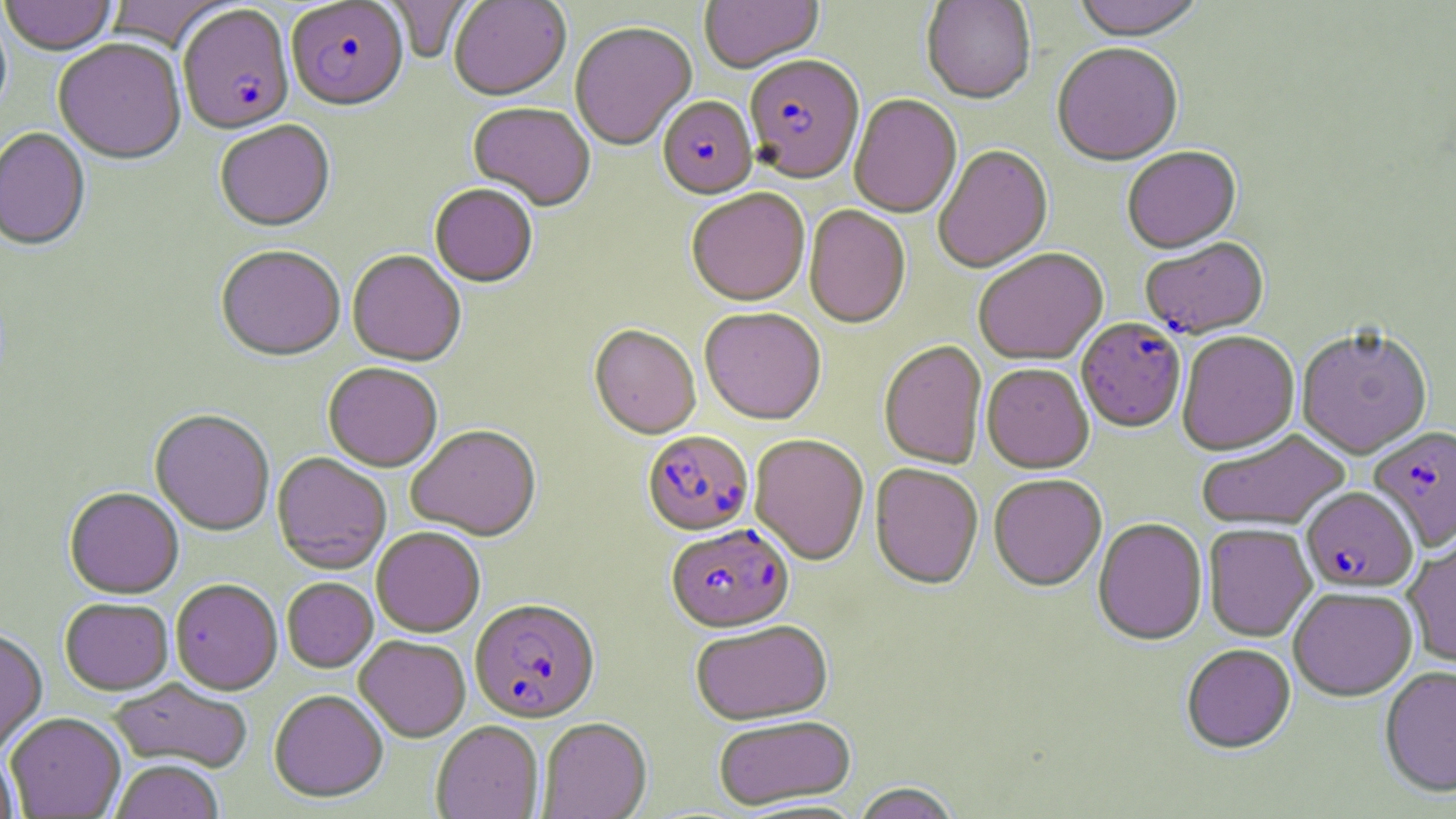
Approximate bounding boxes as named x1/y1/x2/y2 corners in pixels. Plasmodium falciparum-infected red blood cell locations: (x1=287, y1=2, x2=409, y2=114), (x1=178, y1=6, x2=295, y2=137), (x1=744, y1=57, x2=865, y2=186), (x1=657, y1=98, x2=757, y2=201), (x1=1141, y1=239, x2=1269, y2=341), (x1=1077, y1=319, x2=1186, y2=434), (x1=1368, y1=426, x2=1455, y2=553), (x1=642, y1=431, x2=754, y2=536), (x1=1301, y1=487, x2=1418, y2=594), (x1=667, y1=524, x2=794, y2=634), (x1=470, y1=600, x2=600, y2=724). Uninfected red blood cell locations: (x1=0, y1=0, x2=118, y2=57), (x1=107, y1=0, x2=236, y2=53), (x1=384, y1=0, x2=473, y2=62), (x1=449, y1=0, x2=571, y2=102), (x1=700, y1=0, x2=823, y2=75), (x1=921, y1=0, x2=1036, y2=106), (x1=1073, y1=0, x2=1205, y2=44), (x1=570, y1=23, x2=696, y2=152), (x1=53, y1=40, x2=187, y2=167), (x1=1052, y1=44, x2=1184, y2=169), (x1=849, y1=95, x2=962, y2=220), (x1=468, y1=104, x2=595, y2=213), (x1=215, y1=121, x2=335, y2=234), (x1=0, y1=129, x2=91, y2=253), (x1=934, y1=147, x2=1053, y2=274), (x1=1122, y1=148, x2=1242, y2=256), (x1=430, y1=186, x2=538, y2=289), (x1=686, y1=190, x2=810, y2=308), (x1=804, y1=206, x2=911, y2=330), (x1=215, y1=247, x2=345, y2=363), (x1=973, y1=250, x2=1108, y2=367), (x1=348, y1=252, x2=466, y2=367), (x1=699, y1=309, x2=826, y2=427), (x1=589, y1=326, x2=700, y2=440), (x1=1296, y1=330, x2=1432, y2=460), (x1=1177, y1=332, x2=1299, y2=456), (x1=879, y1=341, x2=987, y2=470), (x1=323, y1=364, x2=442, y2=472), (x1=981, y1=365, x2=1094, y2=475), (x1=149, y1=410, x2=275, y2=536), (x1=407, y1=425, x2=541, y2=541), (x1=1197, y1=430, x2=1351, y2=532), (x1=749, y1=435, x2=869, y2=567), (x1=271, y1=453, x2=391, y2=574), (x1=869, y1=464, x2=983, y2=592), (x1=989, y1=476, x2=1107, y2=593), (x1=64, y1=488, x2=184, y2=599), (x1=1093, y1=518, x2=1207, y2=647), (x1=1203, y1=524, x2=1317, y2=642), (x1=372, y1=527, x2=485, y2=637), (x1=1402, y1=534, x2=1456, y2=669), (x1=282, y1=578, x2=378, y2=673), (x1=171, y1=580, x2=282, y2=695), (x1=1289, y1=588, x2=1418, y2=702), (x1=60, y1=598, x2=174, y2=695), (x1=690, y1=621, x2=834, y2=727), (x1=0, y1=629, x2=48, y2=756), (x1=354, y1=636, x2=471, y2=742), (x1=1181, y1=645, x2=1296, y2=756), (x1=1379, y1=667, x2=1456, y2=799), (x1=108, y1=679, x2=253, y2=773), (x1=269, y1=690, x2=388, y2=804), (x1=6, y1=713, x2=126, y2=818), (x1=713, y1=716, x2=857, y2=811), (x1=537, y1=719, x2=652, y2=819), (x1=431, y1=722, x2=544, y2=819), (x1=0, y1=749, x2=19, y2=818), (x1=110, y1=760, x2=224, y2=819), (x1=852, y1=783, x2=961, y2=819). Slide-level diagnosis: Plasmodium falciparum. Thin blood film. One field of a larger specimen. May-Grünwald-Giemsa stain. Captured at 1000x magnification. Optical microscopy. Image is 1456×819 pixels.